Name the parasite shown.
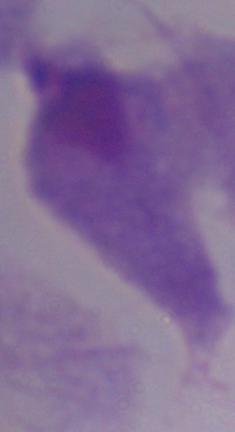

This is a trichomonad.

1000x magnification. Micrograph.